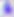

400x magnification. Micrograph. Toxoplasma gondii is shown.